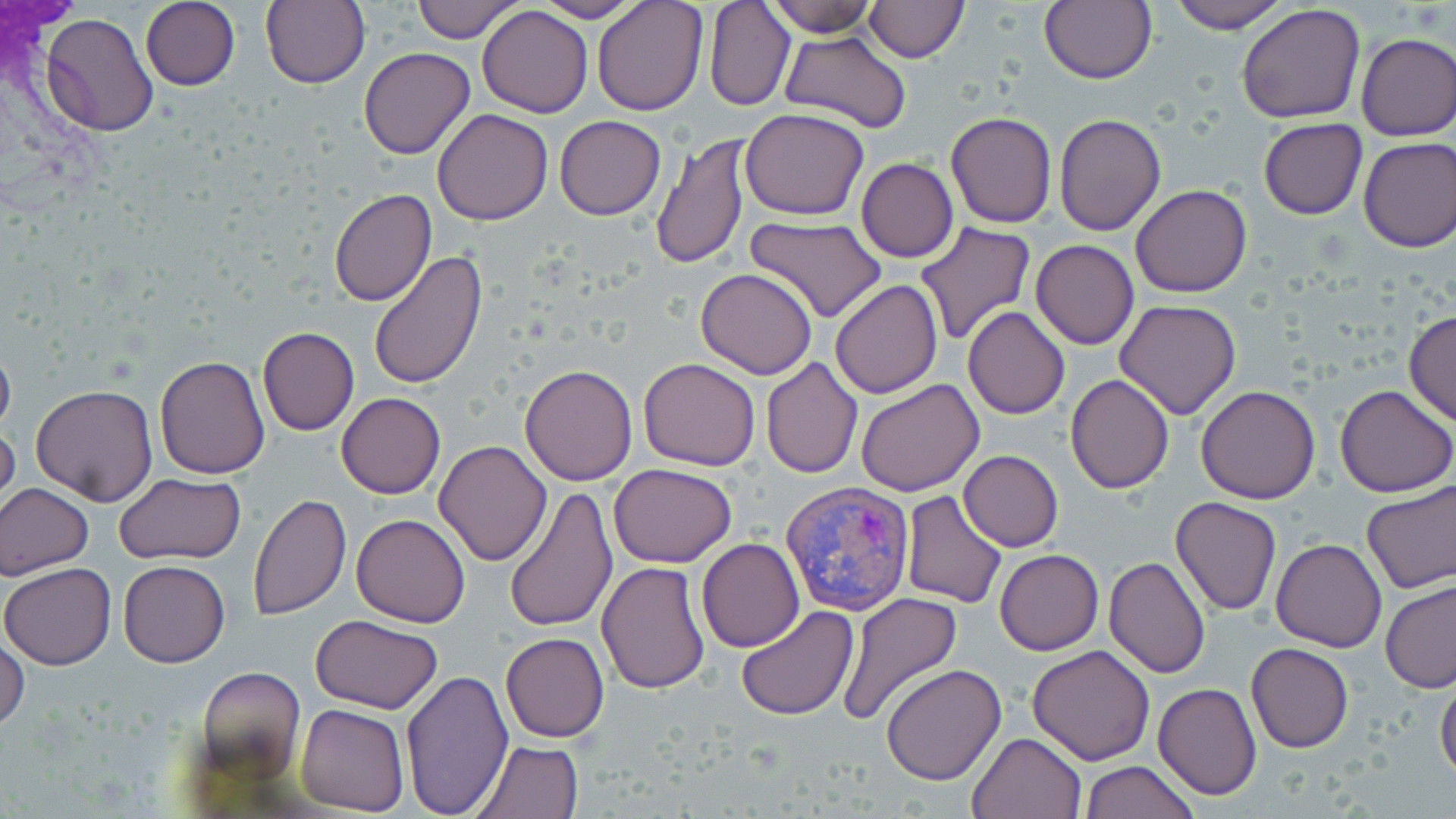

Approximate bounding boxes as [x1, y1, x2, y2] in pixels. Uninfected red blood cell locations: [140, 0, 241, 90], [410, 0, 527, 42], [531, 0, 646, 23], [591, 0, 707, 117], [1040, 0, 1157, 86], [1166, 0, 1292, 33], [260, 1, 369, 89], [767, 1, 877, 36], [862, 1, 969, 64], [703, 2, 795, 111], [1237, 3, 1367, 123], [477, 5, 593, 118], [40, 12, 159, 137], [780, 30, 912, 133], [1356, 32, 1456, 141], [359, 47, 475, 160], [432, 108, 555, 225], [740, 108, 870, 220], [945, 109, 1057, 229], [1053, 113, 1167, 237], [553, 116, 666, 220], [1259, 117, 1366, 220], [650, 133, 751, 270], [1357, 136, 1456, 252], [857, 158, 958, 262], [1131, 184, 1253, 297], [328, 188, 437, 307], [745, 216, 887, 324], [915, 222, 1037, 349], [1030, 240, 1139, 349], [843, 247, 1005, 381], [369, 251, 489, 391], [696, 268, 818, 379], [828, 279, 943, 400], [1114, 300, 1243, 420], [963, 306, 1070, 419], [1404, 310, 1456, 427], [256, 326, 360, 436], [0, 336, 16, 444], [155, 355, 271, 478], [638, 357, 762, 471], [760, 357, 862, 478], [519, 363, 637, 484], [1065, 374, 1175, 493], [856, 379, 983, 497], [30, 384, 159, 506], [1334, 385, 1455, 497], [1195, 386, 1320, 503], [335, 393, 445, 499], [0, 415, 19, 520], [434, 440, 552, 566], [957, 449, 1064, 552], [609, 463, 737, 566], [113, 473, 247, 563], [1361, 478, 1456, 596], [0, 482, 95, 580], [505, 487, 618, 633], [899, 489, 1007, 609], [248, 493, 351, 619], [1170, 496, 1281, 615], [350, 513, 470, 627], [697, 538, 804, 652], [1271, 538, 1386, 652], [995, 549, 1103, 654], [1103, 555, 1212, 679], [119, 560, 231, 666], [597, 561, 710, 694], [1, 563, 117, 670], [1379, 580, 1456, 692], [836, 593, 962, 726], [734, 606, 859, 720], [311, 614, 442, 713], [500, 633, 609, 741], [0, 635, 30, 733], [1245, 642, 1353, 753], [1026, 644, 1157, 765], [880, 663, 1007, 785], [194, 665, 306, 779], [401, 669, 513, 816], [1435, 674, 1456, 782], [1153, 683, 1262, 801], [297, 703, 409, 814], [967, 731, 1089, 819], [472, 739, 584, 819], [1081, 761, 1199, 818]. Plasmodium vivax-infected red blood cell locations: [780, 480, 916, 615]. Slide-level diagnosis: Plasmodium vivax. Image is 1456×819 pixels. One field of a larger specimen. Light microscopy. May-Grünwald-Giemsa stain. Thin blood smear. 1000x magnification.